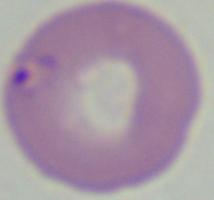

Summary:
  - Modality: photomicrograph
  - Identification: Babesia
  - Magnification: 1000x